Name the blood parasite species.
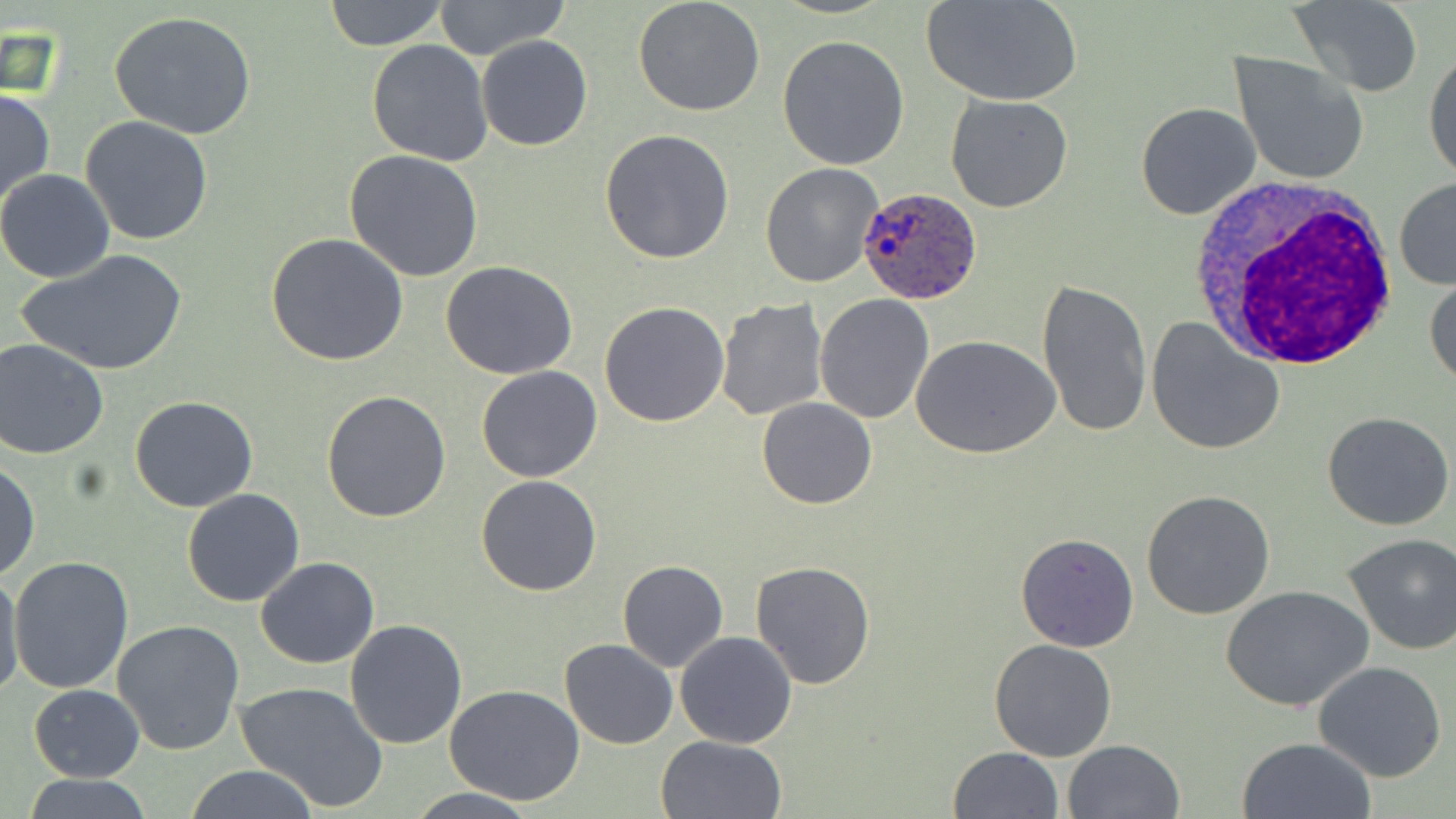

Plasmodium ovale.

Approximate bounding boxes as [x1, y1, x2, y2] in pixels. Plasmodium ovale-infected red blood cell locations: [857, 185, 984, 304]. White blood cell locations: [1183, 180, 1403, 371]. Uninfected red blood cell locations: [323, 0, 448, 50], [432, 0, 570, 62], [923, 0, 1080, 108], [632, 1, 766, 117], [1288, 1, 1424, 96], [110, 11, 258, 141], [477, 35, 593, 151], [777, 36, 909, 172], [367, 40, 493, 168], [1423, 47, 1456, 186], [1229, 51, 1369, 187], [0, 88, 54, 210], [945, 94, 1074, 213], [1134, 101, 1262, 221], [80, 116, 214, 247], [601, 130, 735, 264], [344, 150, 484, 282], [760, 163, 883, 288], [0, 169, 115, 283], [1393, 177, 1456, 290], [265, 232, 409, 367], [17, 249, 188, 377], [440, 260, 578, 380], [1425, 273, 1456, 391], [1036, 278, 1153, 438], [815, 294, 934, 424], [714, 298, 828, 422], [599, 301, 729, 426], [1146, 317, 1285, 454], [914, 336, 1062, 460], [1, 338, 111, 459], [476, 365, 603, 482], [322, 389, 453, 523], [130, 395, 258, 512], [757, 397, 878, 509], [1322, 411, 1455, 531], [0, 459, 40, 581], [476, 474, 602, 595], [182, 487, 305, 607], [1141, 489, 1277, 620], [1016, 532, 1139, 651], [1341, 533, 1456, 655], [7, 555, 135, 694], [257, 557, 380, 669], [750, 559, 877, 688], [617, 560, 729, 671], [0, 566, 24, 706], [1225, 585, 1374, 713], [112, 620, 245, 757], [345, 620, 467, 750], [675, 631, 798, 748], [987, 638, 1117, 760], [558, 640, 678, 750], [1313, 661, 1447, 784], [236, 681, 389, 812], [28, 684, 144, 781], [444, 684, 588, 805], [656, 735, 787, 819], [1234, 736, 1376, 819], [1061, 739, 1185, 819], [947, 746, 1064, 819], [181, 766, 324, 819], [18, 773, 159, 819], [404, 786, 542, 818]. One field of a larger specimen. Thin blood smear. Image is 1456×819 pixels. Captured at 1000x magnification. Light microscopy. May-Grünwald-Giemsa-stained preparation.